Locate every blood parasite and identify its species.
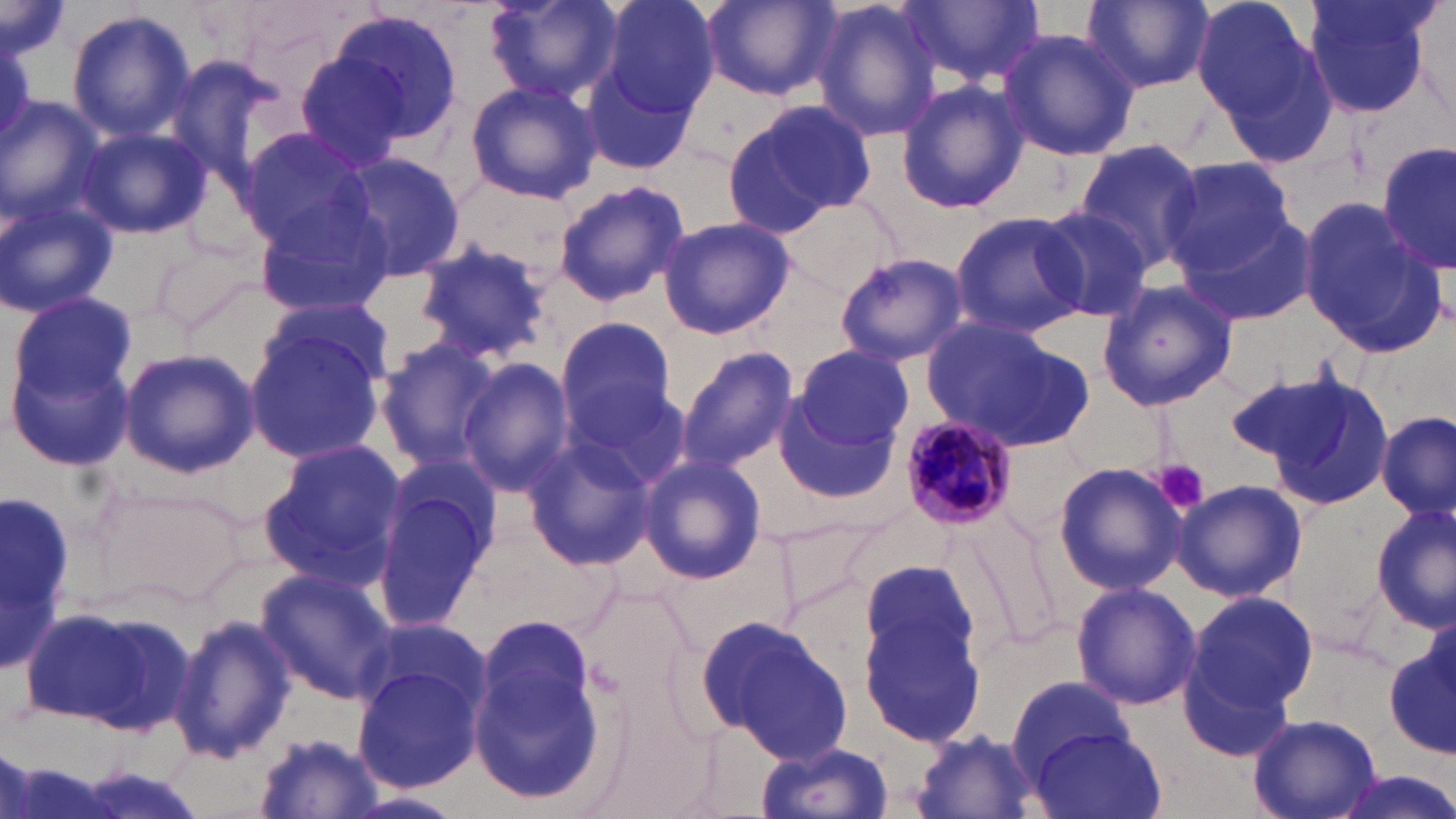

Approximate bounding boxes as [x1, y1, x2, y2] in pixels.
Plasmodium malariae-infected red blood cells: [897, 411, 1020, 529].
No Plasmodium falciparum, Plasmodium ovale, Plasmodium vivax, Babesia divergens, or Trypanosoma brucei observed.

Summary:
  - Platelet locations: [1157, 460, 1210, 514]
  - Uninfected red blood cell locations: [479, 0, 623, 108], [596, 0, 720, 117], [701, 0, 841, 100], [811, 0, 947, 142], [1191, 0, 1328, 136], [1303, 0, 1437, 120], [2, 1, 68, 66], [903, 1, 1043, 89], [1082, 1, 1214, 94], [322, 8, 465, 147], [66, 9, 197, 142], [995, 28, 1139, 161], [289, 44, 425, 172], [162, 52, 291, 193], [581, 54, 704, 176], [464, 79, 602, 203], [896, 81, 1029, 214], [0, 96, 107, 228], [723, 98, 879, 234], [74, 123, 211, 240], [234, 126, 377, 251], [1073, 139, 1205, 272], [1379, 141, 1454, 278], [337, 152, 468, 280], [1160, 155, 1298, 275], [553, 179, 690, 306], [776, 194, 903, 298], [0, 196, 118, 319], [251, 196, 397, 319], [1299, 202, 1442, 355], [1034, 204, 1157, 321], [949, 209, 1090, 337], [1175, 213, 1316, 325], [658, 216, 794, 339], [412, 240, 554, 363], [835, 251, 968, 366], [1096, 278, 1238, 413], [8, 290, 140, 411], [255, 295, 399, 395], [553, 317, 680, 444], [920, 318, 1091, 452], [242, 322, 388, 464], [544, 330, 677, 552], [375, 336, 504, 471], [792, 344, 913, 453], [118, 346, 260, 477], [677, 347, 800, 471], [7, 351, 134, 471], [458, 359, 576, 495], [1224, 366, 1356, 474], [1263, 368, 1394, 509], [563, 379, 689, 491], [772, 392, 903, 509], [1377, 412, 1454, 522], [521, 437, 657, 570], [258, 439, 409, 587], [637, 454, 767, 584], [1051, 460, 1185, 597], [370, 472, 496, 630], [1171, 479, 1307, 603], [0, 492, 75, 677], [1372, 501, 1454, 632], [958, 503, 1065, 649], [852, 563, 987, 748], [254, 568, 394, 704], [1069, 582, 1202, 711], [1182, 587, 1319, 727], [24, 601, 199, 737], [169, 612, 296, 766], [469, 613, 606, 809], [703, 617, 854, 762], [357, 620, 492, 723], [1386, 624, 1456, 763], [354, 665, 483, 793], [1006, 674, 1132, 779], [1249, 714, 1381, 819], [1029, 727, 1168, 819], [912, 731, 1039, 818], [254, 733, 382, 817], [757, 742, 894, 819], [1325, 770, 1456, 819], [348, 791, 464, 819]
  - Slide-level diagnosis: Plasmodium malariae
  - Image size: 1456×819 pixels
  - Stain: May-Grünwald-Giemsa
  - Preparation: thin blood film
  - Field of view: single
  - Modality: light microscopy
  - Magnification: 1000x